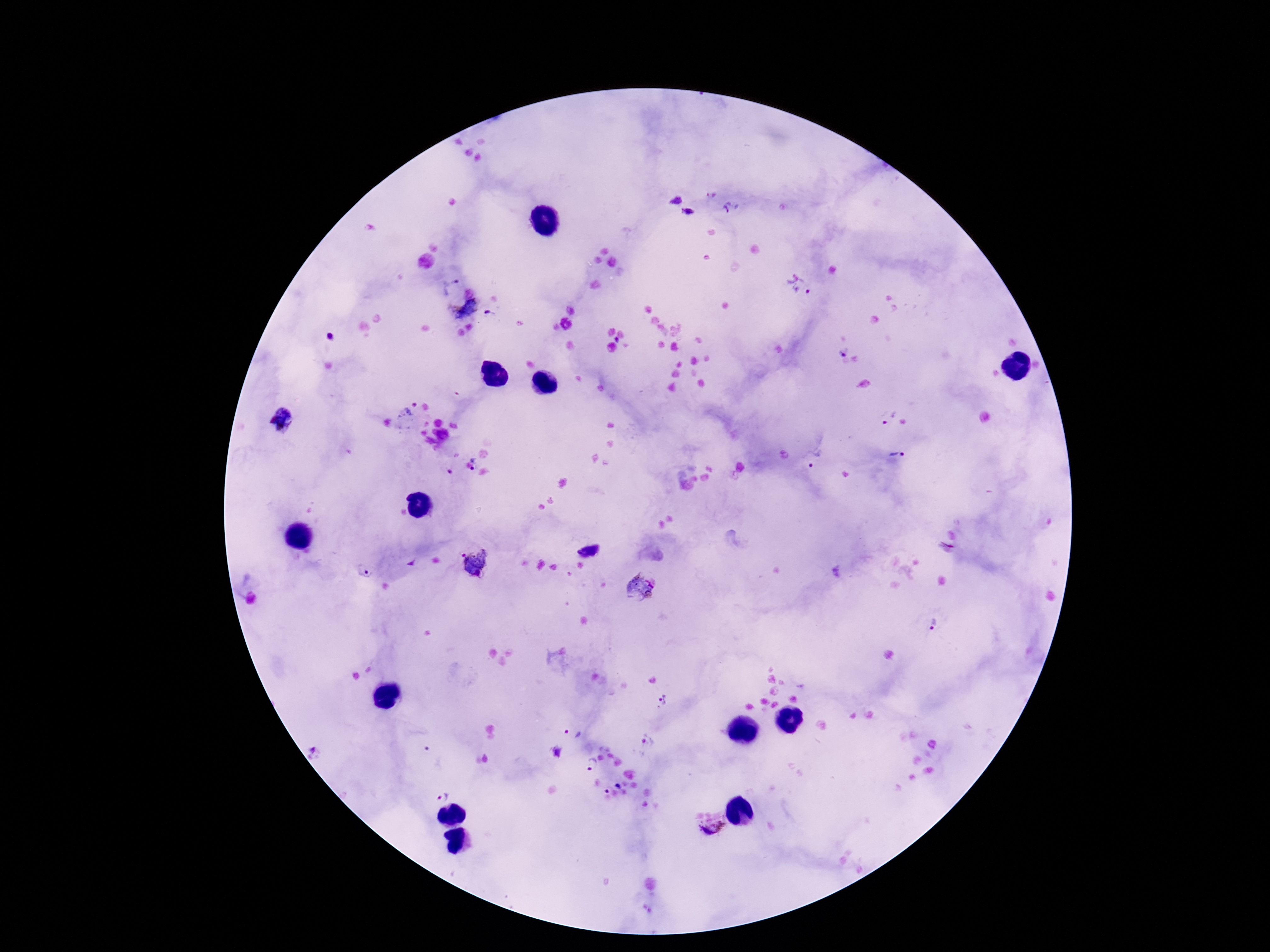 Approximate centers as (x, y) in pixels. Plasmodium parasite locations: (710, 195), (675, 198), (732, 209), (688, 212), (450, 285), (811, 285), (463, 307), (491, 315), (330, 337), (840, 352), (407, 412), (886, 417), (290, 418), (897, 455), (816, 461), (476, 463), (589, 551), (482, 564), (364, 572), (643, 587), (932, 623), (663, 699), (573, 732), (649, 740), (557, 752), (318, 753), (432, 757), (591, 764), (617, 785), (442, 795), (712, 829). Patient malaria status: positive. One field from this slide. Thick peripheral-blood smear. Image is 1270×952 pixels. 100x magnification. Giemsa-stained preparation. Smartphone photograph taken through the microscope eyepiece.